Report the malaria status of this cell.
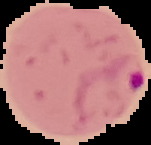
It is parasitized.

Summary:
  - Image type: cell region segmented out of the field of view; surrounding area masked to black
  - Preparation: thin blood smear
  - Image size: 151×145 pixels